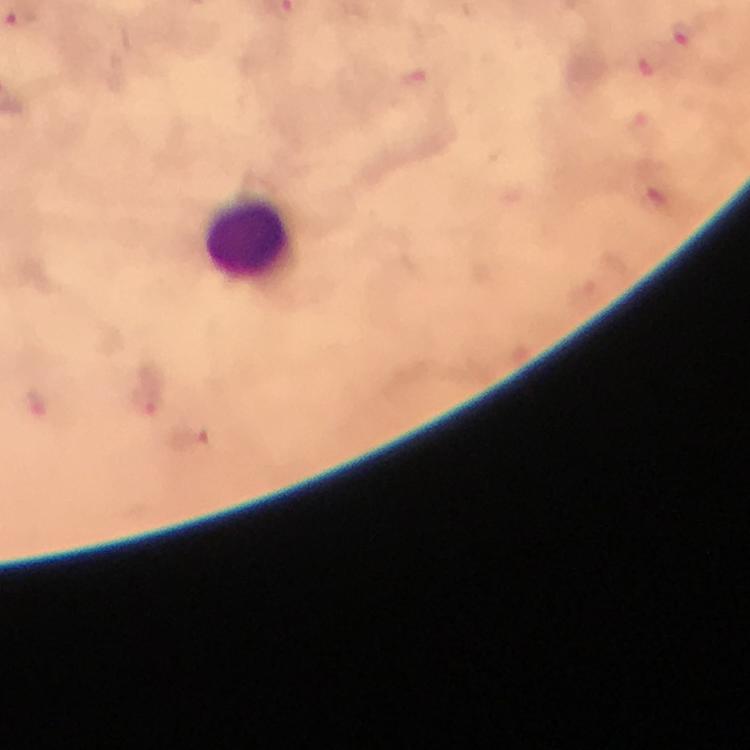
Approximate centers as (x, y) in pixels. Plasmodium parasite locations: (22, 17), (683, 35), (144, 403), (35, 406). Leukocyte locations: (247, 238). At 100x magnification. Smartphone photograph taken through a microscope. From a diagnostic examination for malaria. Giemsa-stained preparation. Cropped region of a single field of view. Immersion oil applied. Image is 750×750 pixels. Thick blood smear.